Classify this cell by malaria status.
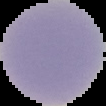

It is uninfected.

From a thin blood smear. Image is 106×106 pixels. Segmented cell region on a black background.